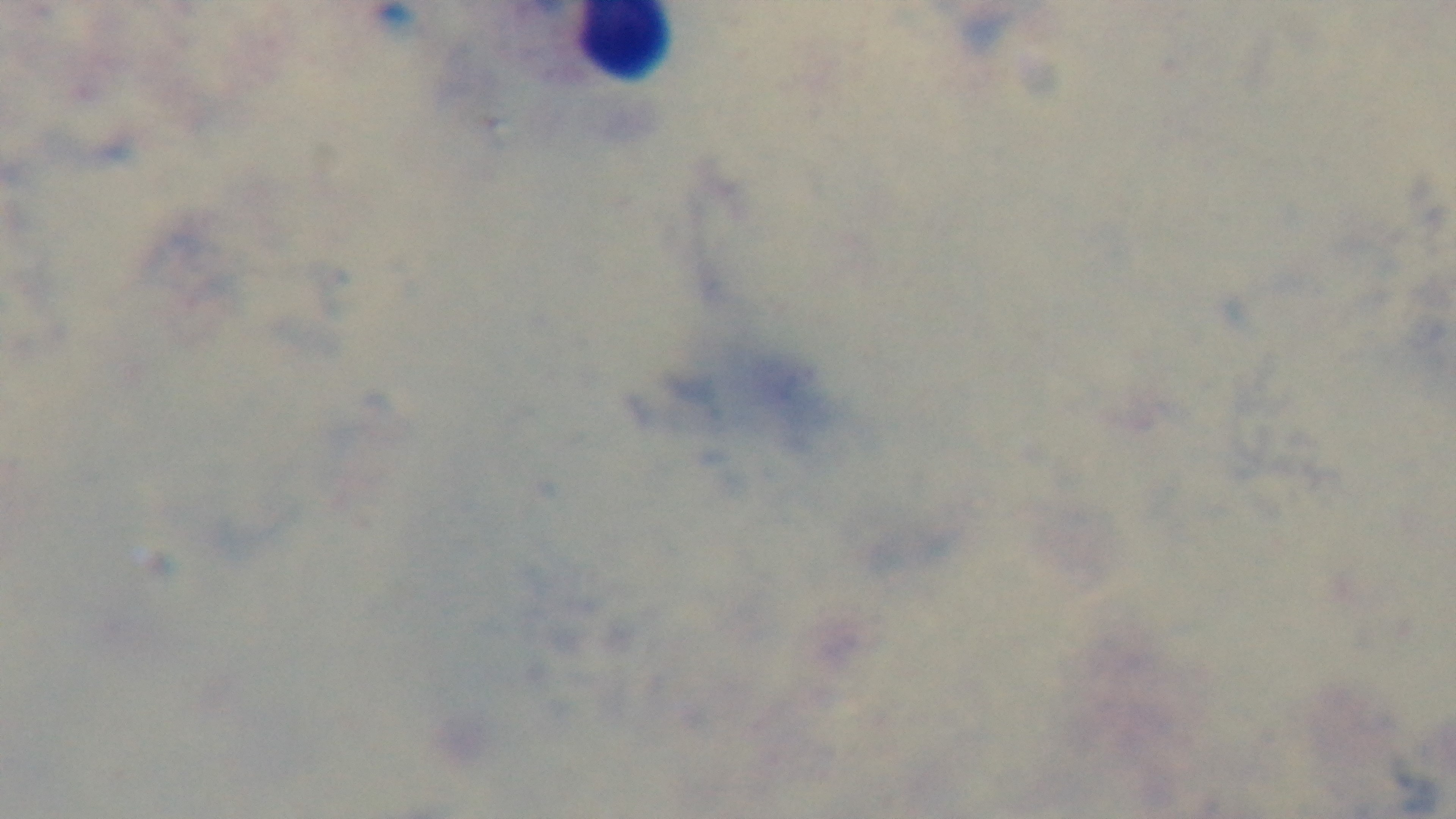
Summary:
  - Objective: 100x oil immersion
  - Capture: mounted 4K digital camera
  - Malaria status: uninfected
  - Preparation: thick blood film
  - Field of view: one from the slide
  - Stain: Giemsa
  - Modality: light microscopy